Give the position of every malaria parasite.
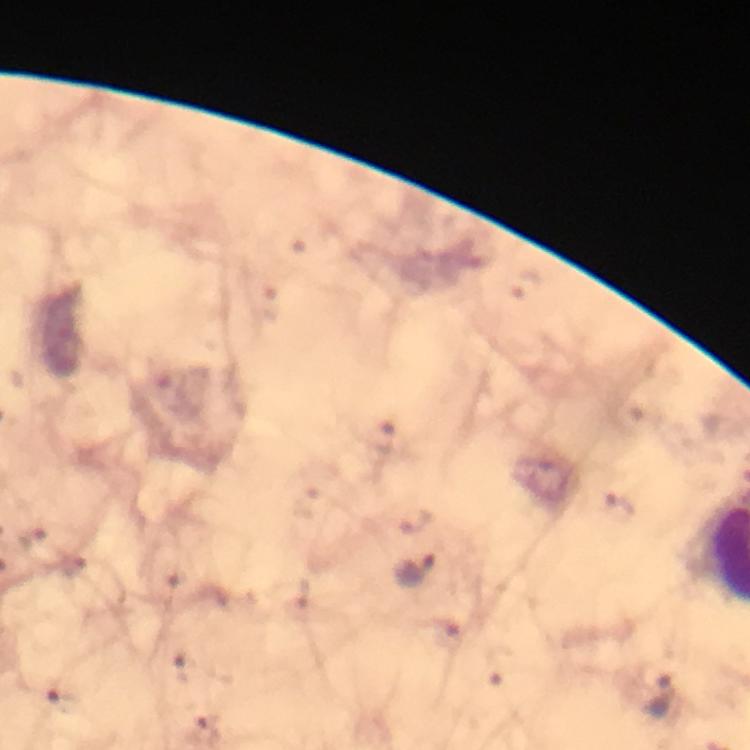
Approximate centers as (x, y) in pixels.
Malaria parasites: (416, 570), (660, 697).

image_size: 750×750 pixels
preparation: thick smear
cropped_from: one field of view
stain: Giemsa
magnification: 100x
immersion_oil: used
capture: smartphone camera through the microscope
context: from a malaria diagnostic workup